Classify this cell by malaria status.
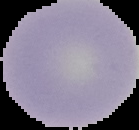
Uninfected.

{
  "image_type": "cell region segmented out of the field of view; surrounding area masked to black",
  "image_size": "139×130 pixels",
  "preparation": "thin blood smear"
}